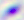 Micrograph. Toxoplasma gondii is seen. 400x magnification.